Outline each Plasmodium falciparum-infected red blood cell.
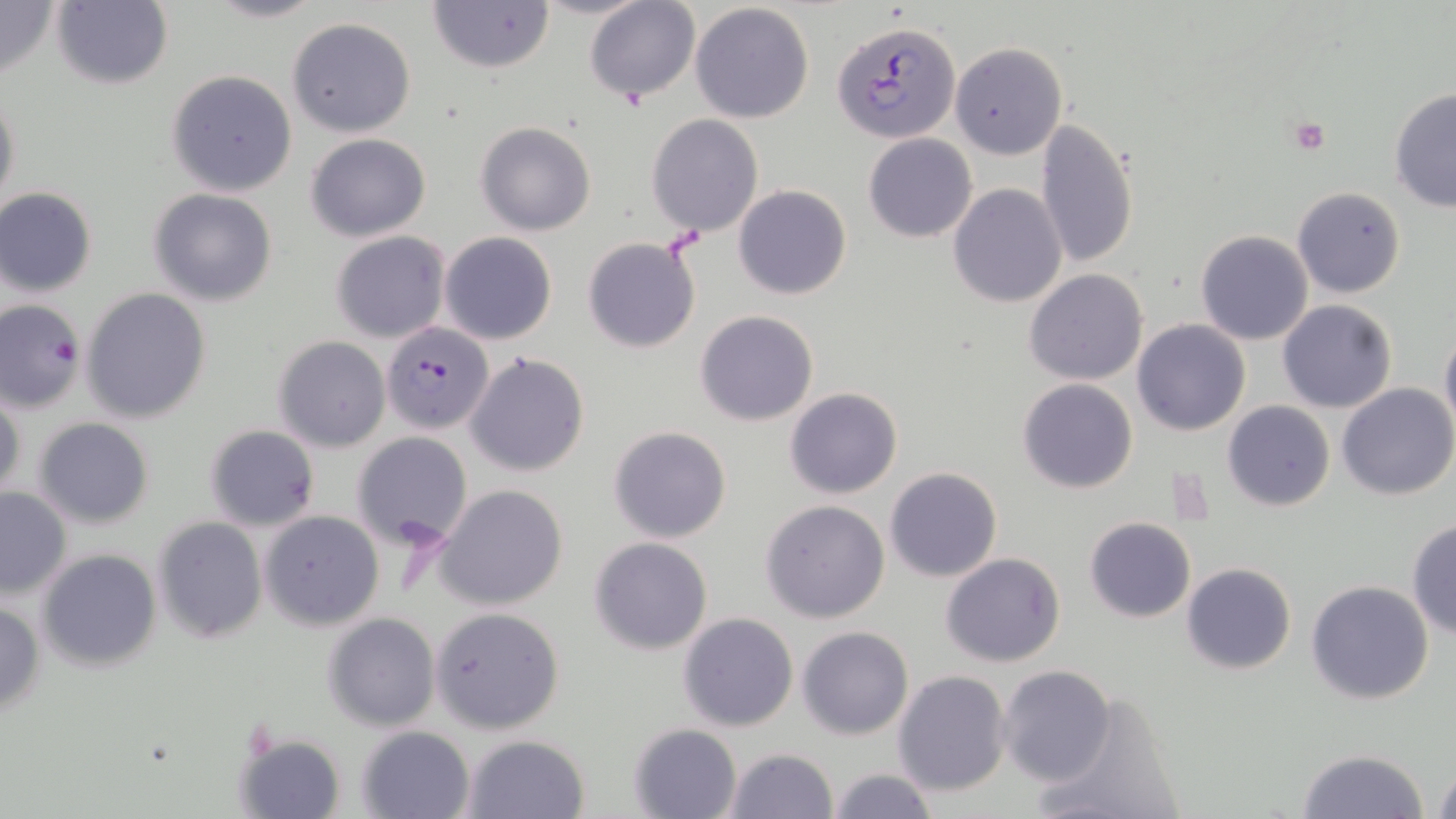

Approximate bounding boxes as (x1,y1)-(x2,y2) corner pairs in pixels.
Plasmodium falciparum-infected red blood cells: (832,20)-(959,142), (1,299)-(85,412), (382,322)-(493,433).

Platelet locations: (1286,116)-(1333,156). Uninfected red blood cell locations: (0,0)-(58,86), (53,0)-(173,89), (204,0)-(327,23), (428,0)-(554,72), (585,2)-(700,104), (690,3)-(815,122), (286,17)-(417,137), (948,41)-(1066,161), (166,70)-(297,196), (1389,87)-(1456,213), (1,88)-(20,215), (645,114)-(765,237), (1034,120)-(1139,269), (477,122)-(596,235), (305,132)-(432,241), (863,133)-(978,242), (949,183)-(1068,307), (733,185)-(852,299), (1291,186)-(1406,297), (0,187)-(98,297), (148,189)-(278,307), (332,230)-(451,343), (1196,230)-(1312,345), (440,232)-(557,345), (582,236)-(703,353), (1024,268)-(1149,385), (80,288)-(212,424), (1277,299)-(1398,414), (696,310)-(817,426), (1133,320)-(1252,437), (1439,325)-(1456,439), (275,337)-(389,452), (465,352)-(592,477), (1017,378)-(1139,494), (1336,383)-(1455,499), (785,387)-(903,498), (0,389)-(24,506), (1222,400)-(1334,512), (33,418)-(155,528), (205,425)-(319,531), (609,425)-(731,543), (352,432)-(473,550), (884,467)-(1002,582), (434,484)-(569,610), (0,485)-(72,599), (760,499)-(891,623), (260,510)-(384,630), (152,516)-(268,644), (1084,517)-(1196,622), (1405,518)-(1456,638), (589,536)-(714,655), (39,549)-(162,670), (941,552)-(1066,668), (1181,562)-(1296,676), (1305,580)-(1434,704), (0,598)-(46,716), (430,606)-(564,734), (322,612)-(440,732), (679,612)-(797,731), (798,626)-(913,740), (998,664)-(1117,787), (892,671)-(1013,795), (1033,688)-(1190,819), (628,723)-(743,818), (356,726)-(474,818), (235,733)-(345,819), (462,733)-(590,819), (721,748)-(837,819), (1297,749)-(1430,819), (1431,757)-(1456,817), (825,767)-(940,819). Slide-level diagnosis: Plasmodium falciparum. Image is 1456×819 pixels. Thin blood film. May-Grünwald-Giemsa stain. Optical microscopy. Captured at 1000x magnification. One field of a larger specimen.